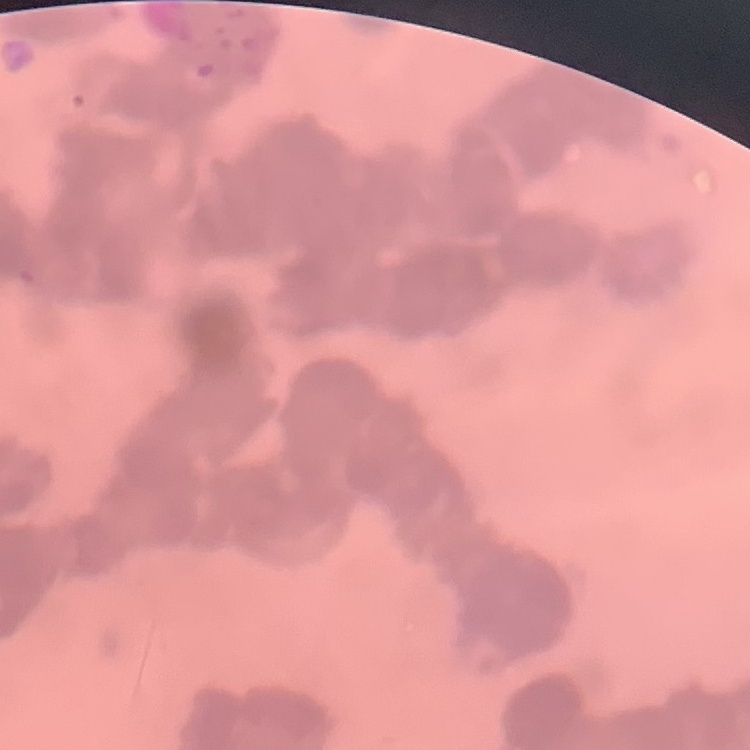
Summary:
  - Red blood cell morphology: rouleaux formation
  - Stain: Field's or Giemsa
  - Preparation: thin peripheral smear
  - Image type: square crop of a larger photomicrograph